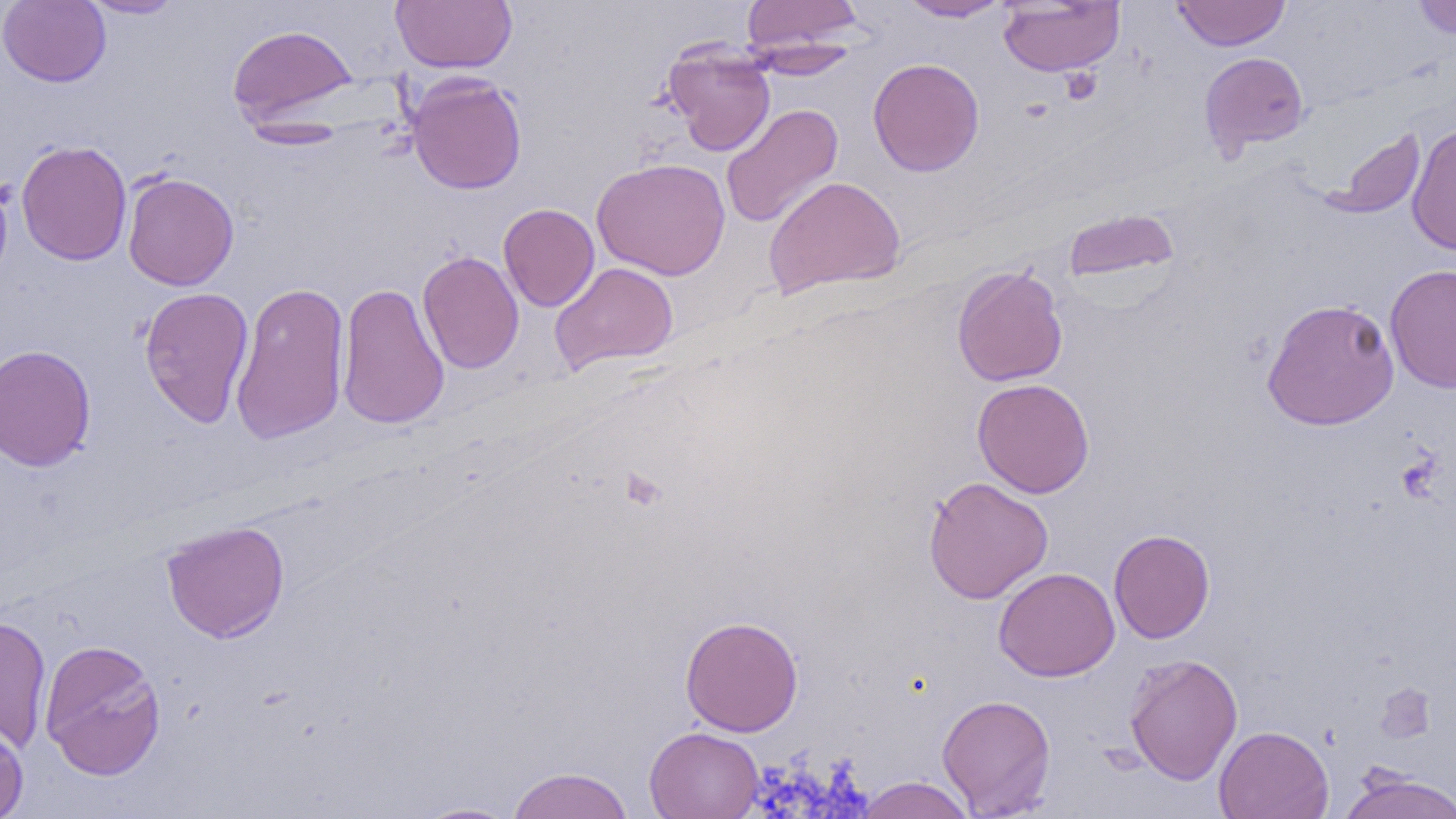
Summary:
  - Coordinate format: approximate bounding boxes as [x1, y1, x2, y2] in pixels
  - Uninfected red blood cell locations: [0, 0, 111, 87], [78, 0, 187, 19], [391, 0, 517, 72], [897, 0, 1012, 22], [1171, 0, 1290, 50], [1412, 0, 1456, 39], [741, 1, 864, 55], [998, 1, 1124, 76], [227, 24, 359, 129], [742, 40, 861, 80], [662, 42, 776, 157], [1199, 52, 1309, 157], [868, 58, 984, 176], [406, 73, 527, 195], [720, 103, 843, 229], [1407, 121, 1456, 256], [1325, 127, 1426, 219], [15, 140, 132, 265], [591, 158, 731, 280], [0, 171, 14, 291], [122, 171, 239, 290], [763, 175, 905, 299], [499, 203, 599, 312], [1062, 208, 1179, 287], [417, 250, 524, 374], [550, 261, 679, 375], [1385, 264, 1456, 393], [952, 265, 1068, 387], [230, 281, 350, 445], [336, 281, 449, 430], [138, 286, 254, 428], [1261, 298, 1400, 430], [0, 343, 97, 471], [971, 378, 1095, 498], [923, 476, 1053, 604], [161, 520, 290, 643], [1109, 528, 1215, 644], [993, 567, 1120, 682], [0, 614, 52, 754], [679, 616, 804, 736], [39, 639, 166, 780], [1123, 652, 1243, 785], [1376, 684, 1437, 744], [937, 694, 1057, 817], [0, 718, 29, 819], [1214, 725, 1334, 819], [644, 726, 764, 819], [505, 766, 635, 819], [1338, 769, 1455, 819], [854, 776, 976, 819], [410, 801, 523, 819]
  - Platelet locations: [1058, 68, 1102, 104], [619, 469, 666, 510]
  - Slide-level diagnosis: negative for blood parasites
  - Modality: light microscopy
  - Image size: 1456×819 pixels
  - Field of view: single
  - Magnification: 1000x
  - Preparation: thin blood smear